Name the parasite shown.
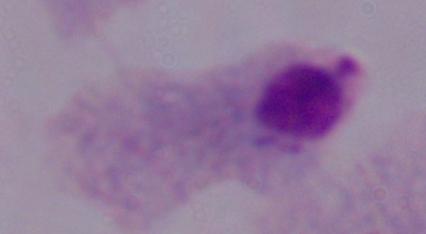
This is a trichomonad.

1000x magnification. Photomicrograph.